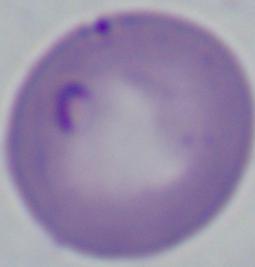
Summary:
  - Identification: Babesia
  - Magnification: 1000x
  - Modality: micrograph